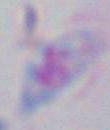
Summary:
  - Identification: Toxoplasma gondii
  - Magnification: 1000x
  - Modality: photomicrograph